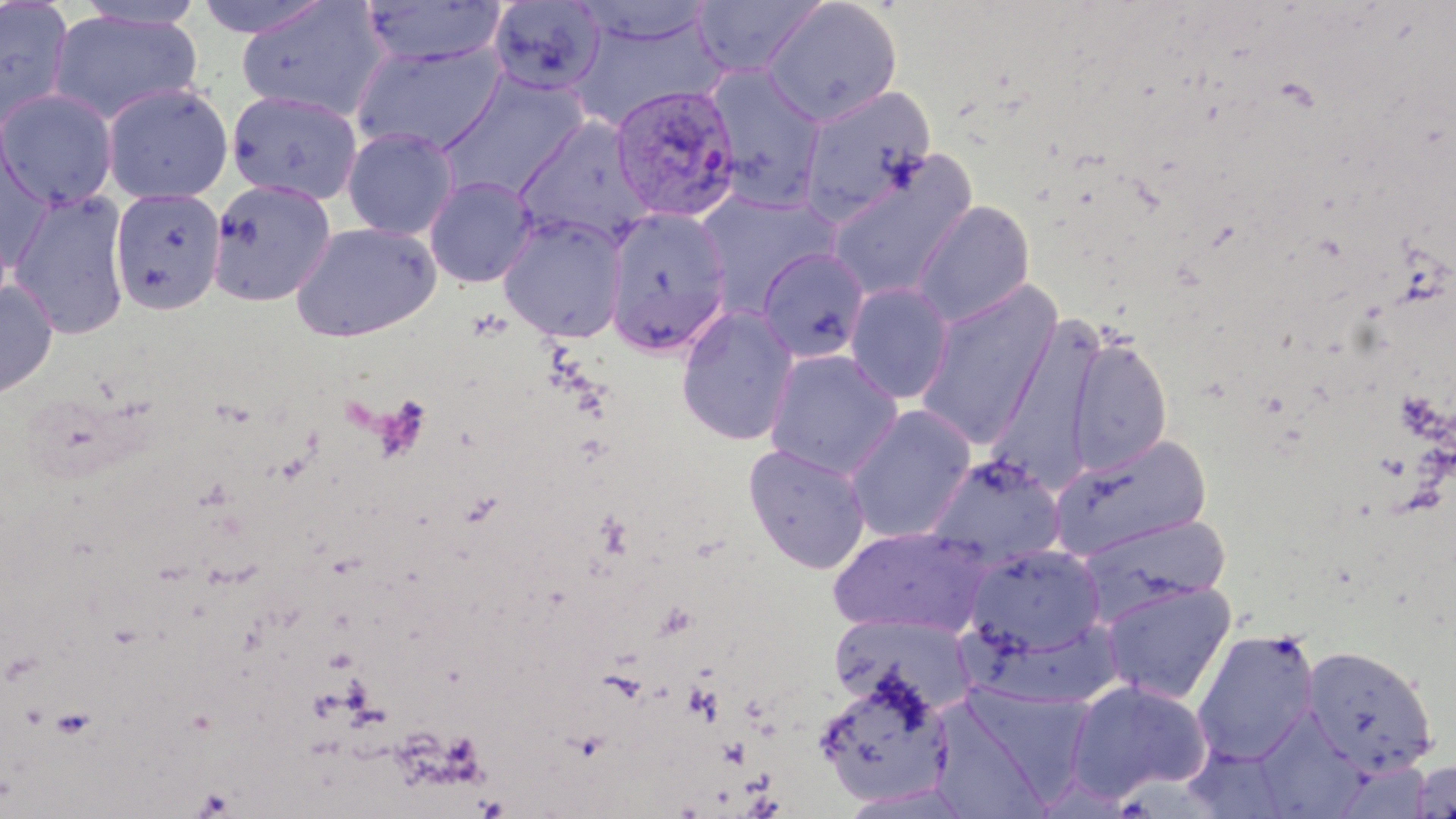
Approximate bounding boxes as named x1/y1/x2/y2 corners in pixels. Plasmodium vivax-infected red blood cell locations: (x1=609, y1=83, x2=742, y2=223). Uninfected red blood cell locations: (x1=73, y1=0, x2=206, y2=32), (x1=190, y1=0, x2=334, y2=40), (x1=359, y1=0, x2=507, y2=68), (x1=690, y1=0, x2=827, y2=79), (x1=761, y1=0, x2=903, y2=126), (x1=487, y1=1, x2=607, y2=96), (x1=569, y1=1, x2=718, y2=46), (x1=0, y1=2, x2=75, y2=131), (x1=236, y1=2, x2=388, y2=122), (x1=47, y1=9, x2=204, y2=126), (x1=562, y1=12, x2=724, y2=133), (x1=350, y1=40, x2=509, y2=157), (x1=704, y1=65, x2=827, y2=213), (x1=436, y1=73, x2=589, y2=201), (x1=100, y1=82, x2=234, y2=205), (x1=796, y1=85, x2=936, y2=223), (x1=1, y1=88, x2=119, y2=210), (x1=226, y1=89, x2=364, y2=205), (x1=512, y1=115, x2=657, y2=249), (x1=341, y1=126, x2=461, y2=241), (x1=0, y1=131, x2=55, y2=269), (x1=825, y1=156, x2=977, y2=304), (x1=424, y1=175, x2=538, y2=288), (x1=206, y1=178, x2=337, y2=307), (x1=109, y1=188, x2=227, y2=315), (x1=694, y1=189, x2=841, y2=315), (x1=8, y1=190, x2=133, y2=339), (x1=911, y1=201, x2=1035, y2=327), (x1=604, y1=206, x2=733, y2=355), (x1=497, y1=213, x2=628, y2=343), (x1=289, y1=221, x2=441, y2=342), (x1=756, y1=247, x2=871, y2=363), (x1=0, y1=278, x2=59, y2=401), (x1=914, y1=280, x2=1063, y2=451), (x1=843, y1=282, x2=955, y2=403), (x1=676, y1=305, x2=800, y2=446), (x1=988, y1=317, x2=1106, y2=486), (x1=1065, y1=334, x2=1174, y2=476), (x1=763, y1=349, x2=904, y2=479), (x1=844, y1=404, x2=977, y2=543), (x1=1049, y1=433, x2=1213, y2=561), (x1=743, y1=442, x2=871, y2=574), (x1=922, y1=453, x2=1068, y2=570), (x1=1073, y1=513, x2=1232, y2=620), (x1=827, y1=525, x2=989, y2=637), (x1=964, y1=543, x2=1105, y2=657), (x1=1099, y1=579, x2=1237, y2=704), (x1=831, y1=613, x2=979, y2=716), (x1=957, y1=625, x2=1136, y2=714), (x1=1192, y1=628, x2=1319, y2=765), (x1=1301, y1=644, x2=1438, y2=777), (x1=813, y1=668, x2=953, y2=807), (x1=1065, y1=679, x2=1212, y2=801), (x1=967, y1=686, x2=1089, y2=809), (x1=936, y1=702, x2=1054, y2=818), (x1=1263, y1=706, x2=1369, y2=819), (x1=1404, y1=757, x2=1455, y2=818). Platelet locations: (x1=324, y1=646, x2=357, y2=672). Slide-level diagnosis: Plasmodium vivax. Captured at 1000x magnification. Image is 1456×819 pixels. May-Grünwald-Giemsa-stained preparation. Light microscopy. Thin blood film. One field of a larger specimen.